Assess the morphology of the red blood cells.
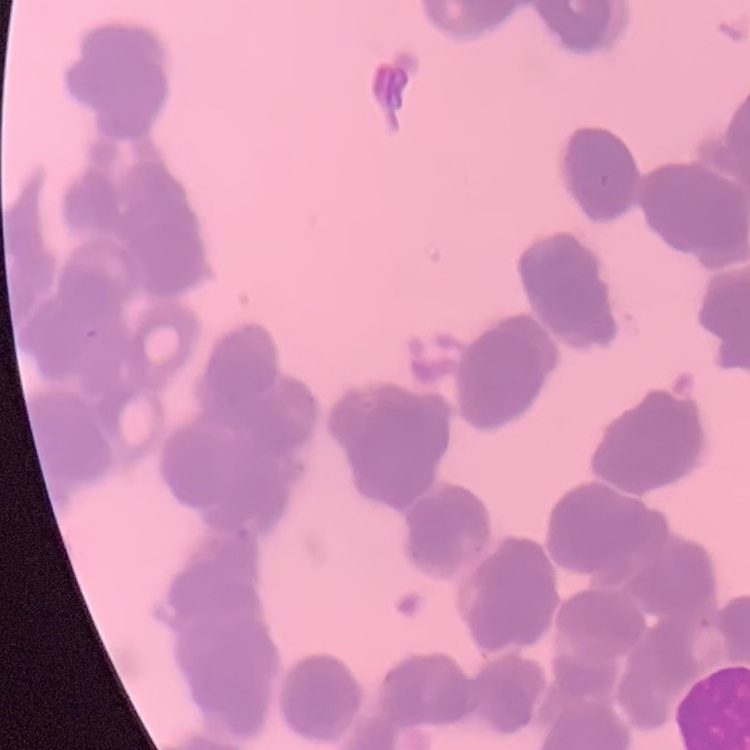
They show rouleaux formation.

Summary:
  - Stain: Field's or Giemsa
  - Preparation: thin blood film
  - Image type: square crop of a larger photomicrograph